Give the extent of all uninfected red blood cells.
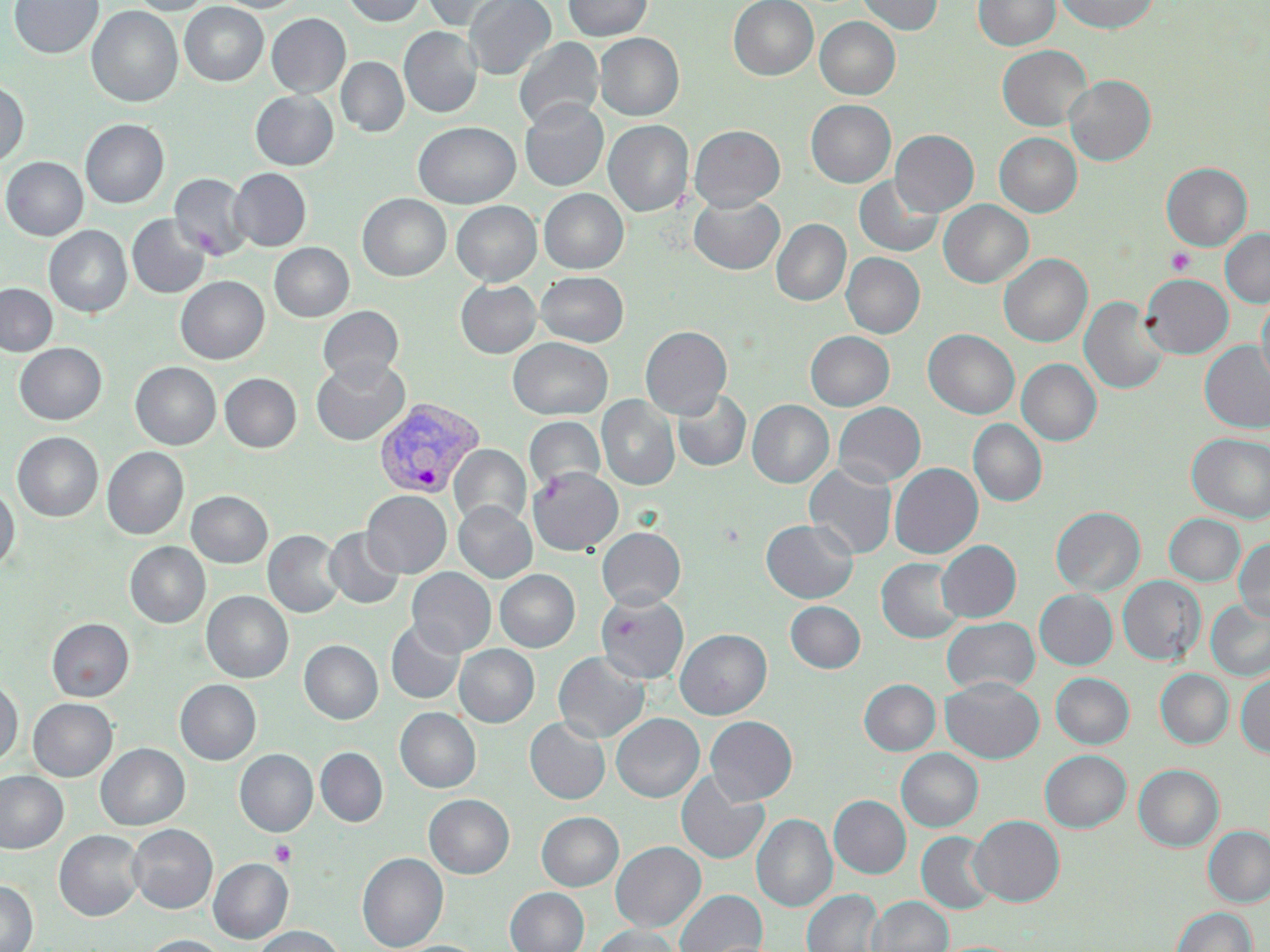
Approximate bounding boxes as (x1, y1, x2, y2) in pixels.
Uninfected red blood cells: (9, 0, 103, 59), (129, 0, 213, 16), (215, 0, 304, 13), (342, 0, 426, 26), (420, 0, 517, 30), (464, 0, 555, 80), (563, 0, 652, 41), (728, 0, 818, 80), (857, 0, 943, 35), (973, 0, 1060, 51), (1055, 0, 1160, 34), (179, 2, 268, 87), (86, 6, 183, 107), (266, 13, 351, 97), (815, 17, 900, 99), (399, 27, 482, 118), (595, 33, 684, 120), (514, 36, 604, 130), (997, 45, 1092, 131), (336, 57, 408, 137), (1064, 75, 1156, 165), (0, 80, 29, 167), (250, 90, 338, 170), (806, 99, 896, 187), (520, 100, 608, 191), (80, 119, 169, 208), (603, 120, 693, 217), (413, 121, 521, 208), (689, 125, 785, 211), (891, 130, 979, 216), (994, 132, 1082, 217), (1, 157, 88, 240), (1161, 162, 1252, 250), (229, 168, 311, 251), (170, 173, 252, 260), (854, 175, 943, 258), (539, 188, 628, 273), (358, 193, 451, 281), (689, 194, 784, 274), (938, 199, 1033, 287), (451, 201, 542, 286), (127, 214, 210, 298), (771, 219, 851, 306), (44, 225, 132, 317), (1220, 229, 1270, 307), (269, 242, 354, 321), (842, 252, 925, 338), (999, 254, 1092, 347), (536, 271, 628, 347), (1141, 274, 1233, 358), (175, 276, 270, 364), (456, 280, 541, 358), (0, 284, 57, 356), (1257, 293, 1270, 390), (1079, 296, 1168, 395), (318, 306, 404, 385), (640, 326, 732, 419), (923, 329, 1020, 419), (806, 331, 894, 410), (508, 337, 612, 420), (1199, 340, 1270, 434), (15, 343, 107, 425), (311, 357, 410, 446), (1017, 359, 1101, 446), (130, 362, 221, 449), (220, 373, 301, 452), (672, 389, 751, 473), (597, 395, 679, 490), (747, 400, 834, 488), (833, 402, 925, 487), (524, 416, 606, 493), (968, 419, 1047, 507), (12, 432, 103, 522), (1187, 433, 1270, 523), (449, 444, 531, 527), (102, 447, 189, 539), (804, 462, 897, 559), (890, 463, 983, 559), (528, 467, 623, 555), (0, 486, 19, 572), (186, 490, 272, 567), (362, 490, 452, 578), (454, 502, 537, 582), (1051, 506, 1144, 596), (1164, 513, 1245, 586), (760, 519, 858, 603), (324, 527, 404, 609), (597, 527, 685, 609), (263, 530, 345, 618), (1233, 538, 1270, 622), (936, 540, 1021, 622), (125, 542, 210, 628), (877, 557, 964, 643), (407, 567, 495, 657), (495, 569, 580, 652), (1118, 576, 1205, 664), (1035, 589, 1117, 669), (202, 591, 293, 683), (596, 592, 689, 685), (1206, 599, 1270, 681), (785, 601, 865, 673), (941, 616, 1040, 695), (46, 618, 134, 702), (386, 620, 465, 704), (675, 629, 772, 719), (299, 640, 383, 724), (454, 644, 539, 727), (553, 652, 650, 742), (1155, 669, 1233, 749), (1051, 673, 1134, 749), (1236, 673, 1270, 758), (941, 677, 1044, 763), (175, 679, 261, 765), (859, 679, 940, 755), (0, 680, 22, 766), (28, 698, 117, 781), (395, 708, 481, 793), (611, 713, 704, 802), (705, 716, 797, 804), (525, 717, 610, 804), (95, 743, 189, 830), (315, 748, 388, 826), (896, 748, 983, 832), (235, 749, 318, 836), (1040, 750, 1131, 832), (1134, 764, 1224, 851), (0, 771, 68, 853), (676, 772, 769, 865), (424, 794, 514, 878), (829, 795, 911, 878), (537, 812, 623, 890), (752, 814, 837, 912), (968, 815, 1065, 907), (128, 824, 217, 914), (1203, 826, 1270, 907), (54, 830, 145, 921), (917, 831, 998, 914), (611, 841, 705, 932), (358, 853, 448, 951), (208, 858, 293, 943), (0, 881, 38, 952), (505, 887, 589, 952), (675, 889, 767, 952), (802, 889, 884, 952), (867, 896, 952, 952), (1171, 907, 1257, 952), (254, 925, 346, 952), (594, 925, 682, 952), (140, 934, 230, 952).

slide-level diagnosis = Plasmodium vivax
preparation = thin blood smear
image size = 1270×952 pixels
field of view = one of a larger specimen
modality = light microscopy
Plasmodium vivax-infected red blood cell locations = approximate bounding boxes as (x1, y1, x2, y2) in pixels: (373, 398, 485, 500)
platelet locations = approximate bounding boxes as (x1, y1, x2, y2) in pixels: (1165, 248, 1195, 276), (270, 839, 296, 867)
magnification = 1000x
stain = May-Grünwald-Giemsa